State which cell type is depicted.
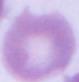

This is an erythrocyte.

Photomicrograph. 1000x magnification.